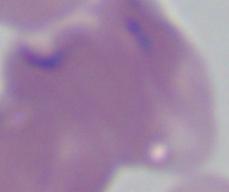 Photomicrograph. Captured at 1000x magnification. A Babesia parasite is shown.